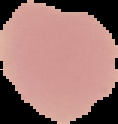
Summary:
  - Result: no Plasmodium parasites detected
  - Image type: segmented cell region on a black background
  - Preparation: thin blood film
  - Image size: 118×124 pixels